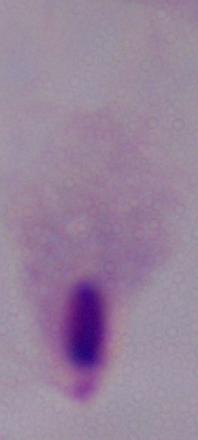

modality: micrograph
identification: trichomonad
magnification: 1000x